Classify this cell by malaria status.
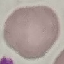

It is uninfected.

Giemsa stain. Cell patch, automatically extracted from a larger field of view and resized to 64 × 64 pixels. Thin smear of blood. Photographed with a smartphone camera at the microscope eyepiece.